Classify this cell by malaria status.
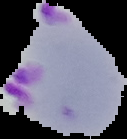
Parasitized.

Summary:
  - Preparation: thin blood film
  - Image type: segmented cell region with the area outside set to black
  - Image size: 127×139 pixels